Locate every Plasmodium falciparum parasite and identify its life-cycle stage.
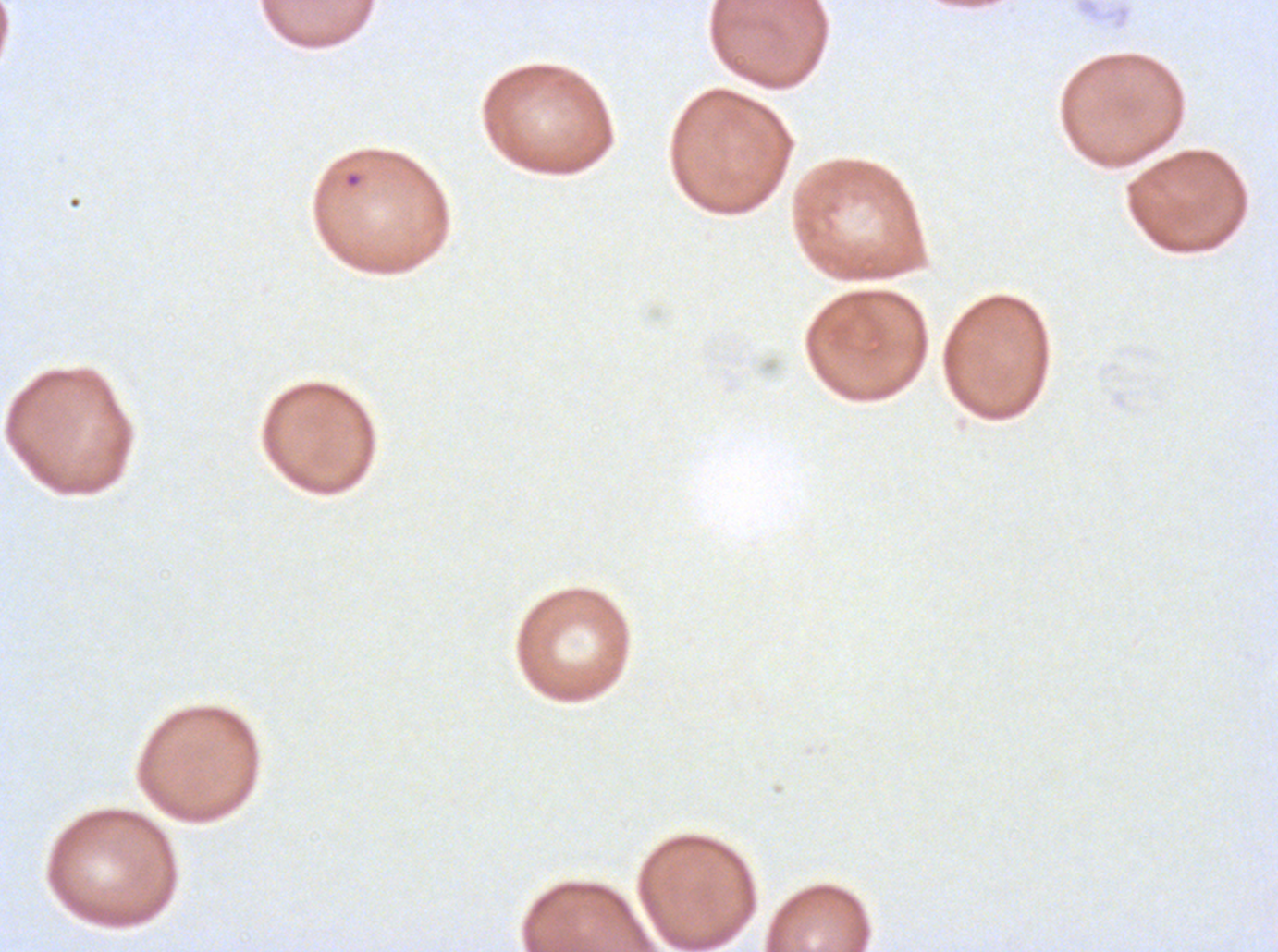
Approximate bounding boxes as [x1, y1, x2, y2] in pixels.
Rings: [343, 171, 363, 189].
No late-ring/early-trophozoite forms, mid trophozoites, late trophozoites, early schizonts, late schizonts, segmenters, or gametocytes observed.

Giemsa stain. A sub-image separated from a larger composite. Ex-vivo Plasmodium falciparum culture from a patient in The Gambia, grown for 24 to 48 hours. Thin blood smear. Image is 1278×952 pixels.